Report the malaria status of this cell.
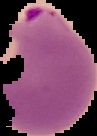

It is parasitized.

{
  "preparation": "thin blood film",
  "image_size": "97×136 pixels",
  "image_type": "segmented cell region with the area outside set to black"
}